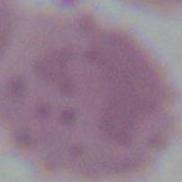

identification = erythrocyte
magnification = 1000x
modality = micrograph